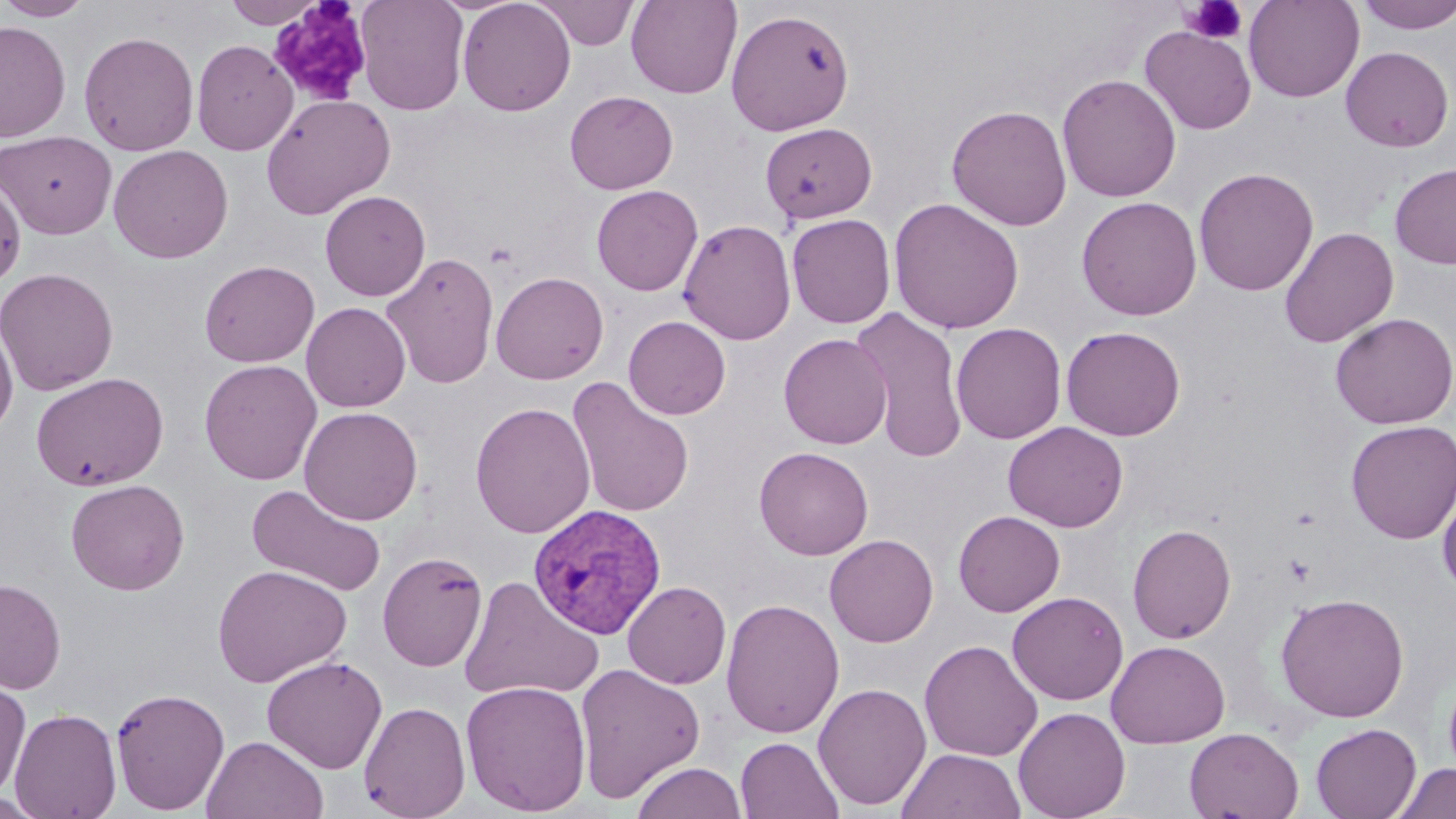
Plasmodium vivax-infected red blood cell locations = approximate bounding boxes as (x1, y1, x2, y2) in pixels: (528, 503, 667, 640)
slide-level diagnosis = Plasmodium vivax
image size = 1456×819 pixels
uninfected red blood cell locations = approximate bounding boxes as (x1, y1, x2, y2) in pixels: (0, 0, 96, 21), (224, 0, 324, 28), (355, 0, 470, 115), (457, 0, 576, 116), (532, 0, 640, 50), (625, 0, 742, 99), (1243, 0, 1364, 102), (1355, 0, 1456, 34), (727, 8, 855, 136), (0, 20, 71, 143), (1139, 25, 1257, 135), (79, 30, 199, 156), (192, 39, 298, 155), (1340, 46, 1453, 152), (1057, 73, 1181, 202), (564, 90, 678, 194), (260, 93, 395, 219), (946, 104, 1072, 231), (760, 122, 877, 223), (1, 130, 117, 239), (108, 144, 233, 264), (1390, 162, 1456, 269), (1193, 167, 1318, 296), (0, 174, 26, 288), (592, 185, 703, 296), (320, 190, 431, 301), (1076, 196, 1202, 320), (888, 197, 1025, 334), (787, 213, 896, 328), (679, 218, 796, 345), (1279, 227, 1399, 348), (381, 251, 500, 390), (199, 259, 319, 367), (0, 267, 119, 396), (490, 271, 609, 384), (301, 302, 411, 412), (851, 306, 970, 463), (1330, 312, 1456, 430), (623, 315, 731, 420), (0, 319, 18, 438), (951, 322, 1067, 445), (1060, 325, 1186, 441), (778, 333, 893, 448), (199, 359, 322, 485), (31, 372, 169, 490), (566, 376, 695, 518), (469, 401, 595, 538), (299, 406, 423, 525), (1003, 421, 1129, 532), (1346, 421, 1456, 544), (753, 446, 873, 560), (65, 479, 190, 595), (245, 483, 387, 597), (1438, 484, 1456, 597), (953, 510, 1065, 616), (1127, 523, 1236, 644), (824, 534, 938, 647), (377, 551, 488, 672), (212, 564, 351, 687), (0, 577, 66, 694), (459, 577, 603, 702), (623, 580, 731, 689), (1007, 591, 1129, 705), (1275, 591, 1410, 723), (721, 598, 844, 738), (1106, 639, 1230, 748), (919, 640, 1043, 761), (261, 656, 387, 774), (574, 663, 706, 803), (1442, 668, 1456, 783), (0, 676, 31, 801), (460, 679, 592, 816), (812, 682, 931, 810), (110, 686, 230, 815), (359, 700, 471, 819), (1013, 706, 1131, 819), (9, 707, 122, 819), (1310, 723, 1421, 819), (1184, 727, 1304, 819), (202, 735, 328, 818), (736, 736, 843, 819), (896, 748, 1026, 819), (631, 761, 748, 819), (1391, 762, 1455, 818), (0, 793, 50, 817)
modality = optical microscopy
preparation = thin blood smear
magnification = 1000x
stain = May-Grünwald-Giemsa
field of view = one of a larger specimen
platelet locations = approximate bounding boxes as (x1, y1, x2, y2) in pixels: (269, 1, 375, 106), (1181, 1, 1248, 44), (1284, 554, 1315, 586)